Evaluate for malaria.
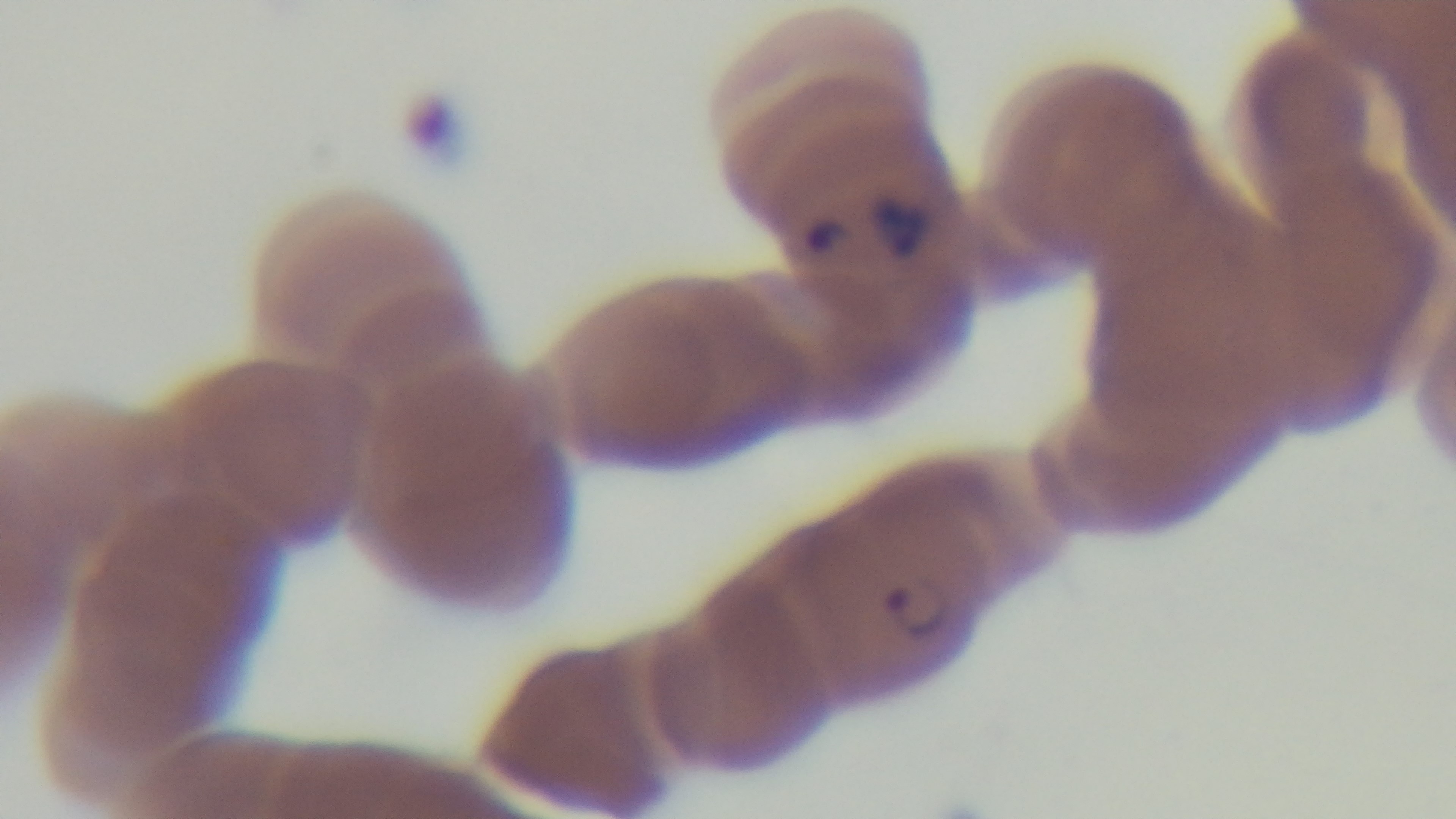
Positive.

Giemsa stain. One field from the slide. Mounted 4K digital camera. 100x oil-immersion objective. Light microscopy. Preparation: thin.